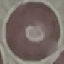
malaria status = uninfected
capture = smartphone camera at the microscope eyepiece
image type = cell patch, automatically extracted from a larger field of view and resized to 64 × 64 pixels
stain = Giemsa
preparation = thin blood smear